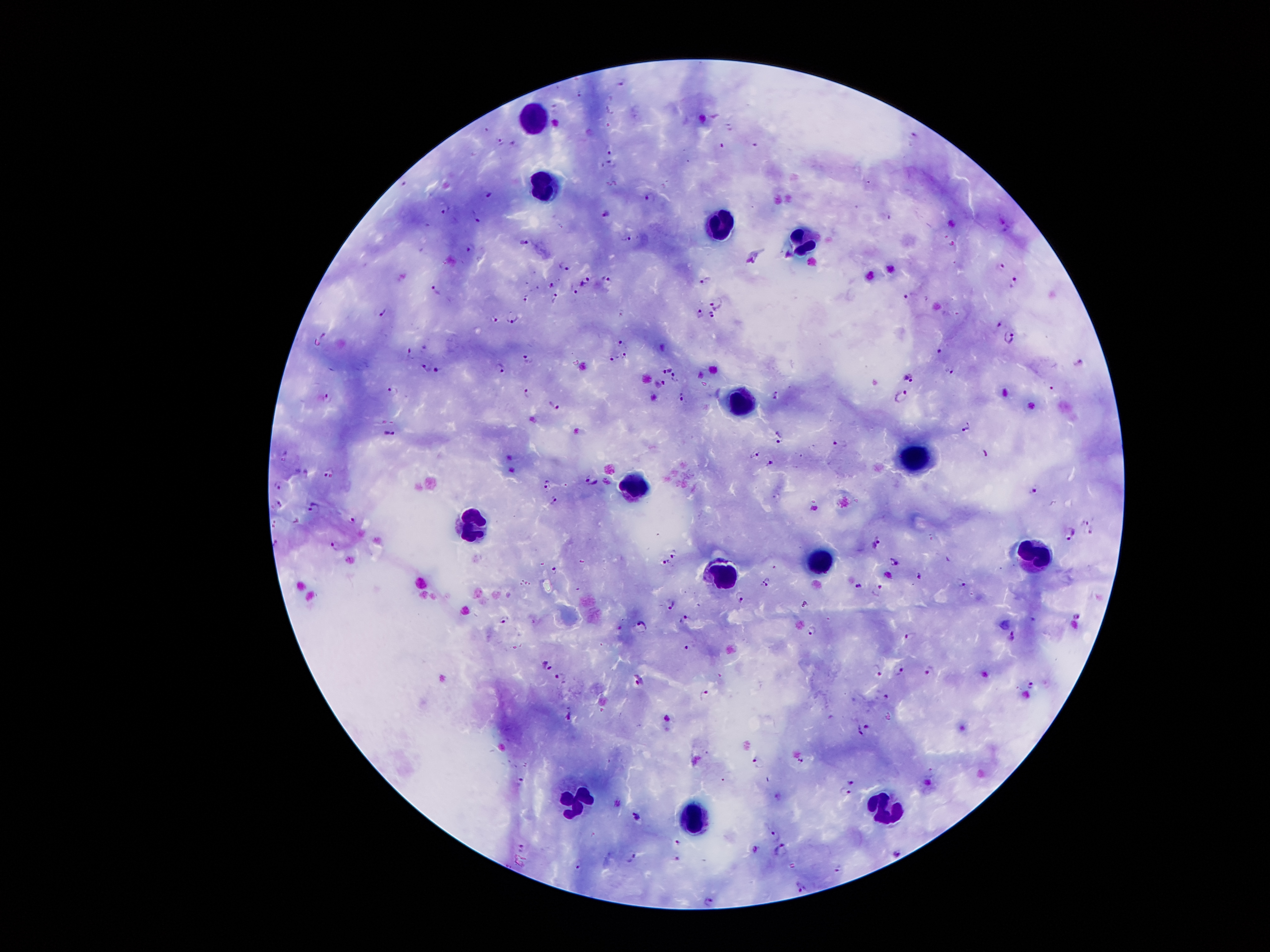

stain: Giemsa
patient_malaria_status: infected with Plasmodium falciparum
capture: smartphone camera through the microscope eyepiece
plasmodium_parasite_locations: 'approximate centers as (x, y) in pixels: (622, 83), (580, 94), (487, 130), (914, 134), (500, 141), (722, 145), (756, 145), (609, 151), (610, 163), (489, 194), (649, 197), (447, 209), (607, 213), (477, 217), (628, 238), (523, 240), (469, 247), (1002, 263), (564, 266), (705, 279), (584, 281), (607, 282), (1012, 282), (552, 284), (574, 288), (436, 290), (907, 293), (555, 297), (526, 298), (715, 298), (697, 309), (383, 312), (711, 316), (512, 318), (494, 320), (1008, 338), (623, 342), (940, 348), (625, 352), (531, 353), (615, 353), (409, 354), (502, 365), (426, 368), (952, 368), (436, 369), (666, 369), (674, 377), (909, 379), (659, 383), (528, 389), (391, 392), (774, 392), (902, 394), (680, 395), (325, 399), (554, 405), (966, 420), (388, 433), (777, 433), (837, 441), (754, 449), (285, 455), (768, 464), (329, 472), (593, 478), (547, 484), (277, 486), (1032, 488), (553, 498), (278, 504), (314, 507), (352, 520), (1085, 520), (1069, 531), (1089, 531), (876, 538), (335, 544), (673, 553), (895, 560), (666, 561), (555, 570), (919, 572), (766, 582), (961, 583), (859, 585), (880, 590), (742, 596), (671, 605), (1076, 616), (502, 618), (685, 618), (641, 626), (812, 628), (909, 637), (1011, 637), (688, 648), (549, 666), (897, 668), (930, 669), (880, 671), (561, 676), (639, 680), (1029, 683), (705, 694), (885, 697), (859, 731), (800, 758), (755, 761), (851, 780), (521, 782), (844, 792), (637, 816), (774, 835), (677, 843), (519, 847), (755, 850), (781, 850), (898, 855), (630, 856), (675, 858), (578, 865), (837, 868), (800, 886), (707, 901)'
magnification: 100x
field_of_view: single
image_size: 1270×952 pixels
preparation: thick blood smear
leukocyte_locations: 'approximate centers as (x, y) in pixels: (531, 123), (546, 183), (723, 224), (807, 242), (740, 404), (911, 455), (632, 486), (471, 523), (1037, 552), (821, 559), (723, 577), (572, 800), (883, 811), (692, 817)'